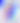 Micrograph. 400x magnification. Toxoplasma gondii is shown.